Report the malaria status of this cell.
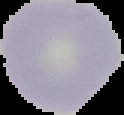

Uninfected.

Summary:
  - Image type: segmented cell region on a black background
  - Image size: 124×115 pixels
  - Preparation: thin blood smear